Assess the morphology of the red blood cells.
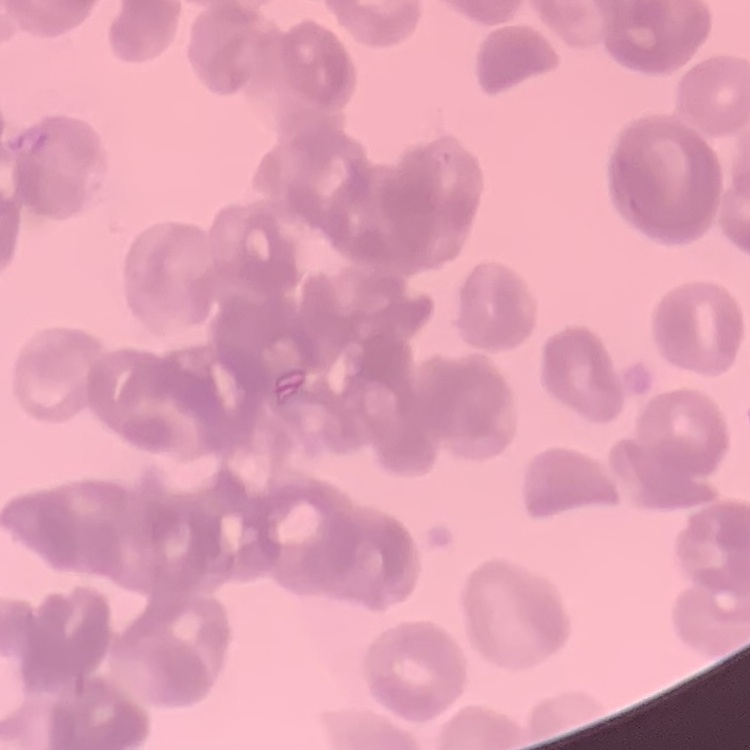
They show rouleaux formation.

Field's or Giemsa stain. Thin peripheral smear. Square crop of a larger photomicrograph.